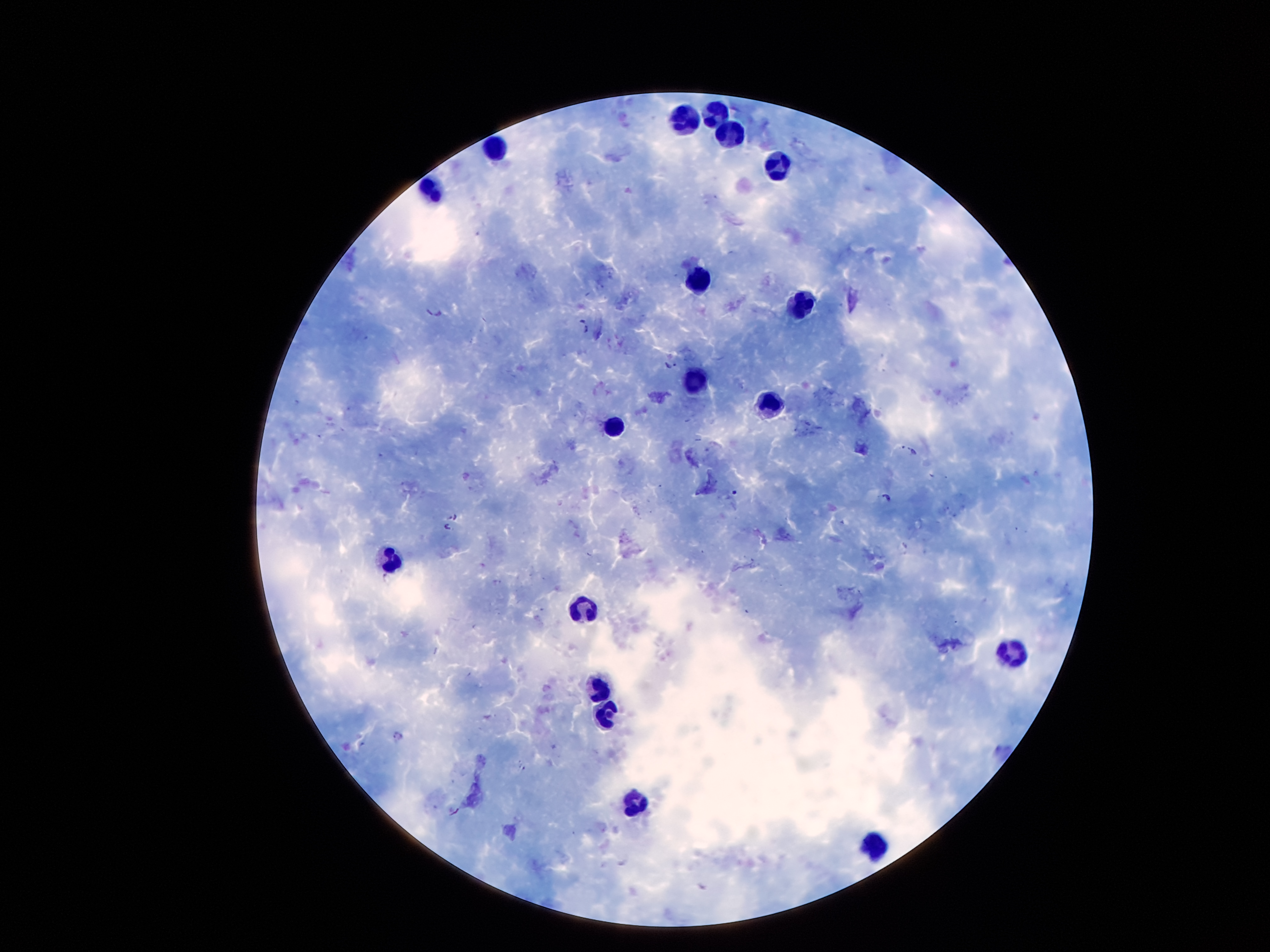 Approximate centers as {x, y} in pixels. Plasmodium parasite locations: {435, 309}, {583, 327}, {671, 364}, {908, 448}, {887, 499}, {454, 516}, {449, 526}, {453, 812}. Leukocyte locations: {717, 121}, {687, 125}, {730, 140}, {496, 148}, {778, 168}, {435, 190}, {700, 283}, {805, 307}, {696, 376}, {769, 411}, {614, 430}, {391, 560}, {583, 611}, {1013, 652}, {599, 686}, {610, 714}, {635, 803}, {872, 851}. Photographed through the microscope eyepiece with a smartphone camera. 100x magnification. Image is 1270×952 pixels. Thick peripheral-blood smear. Giemsa-stained preparation. Patient malaria status: positive for Plasmodium falciparum. Single field of view.